Identify the preparation type.
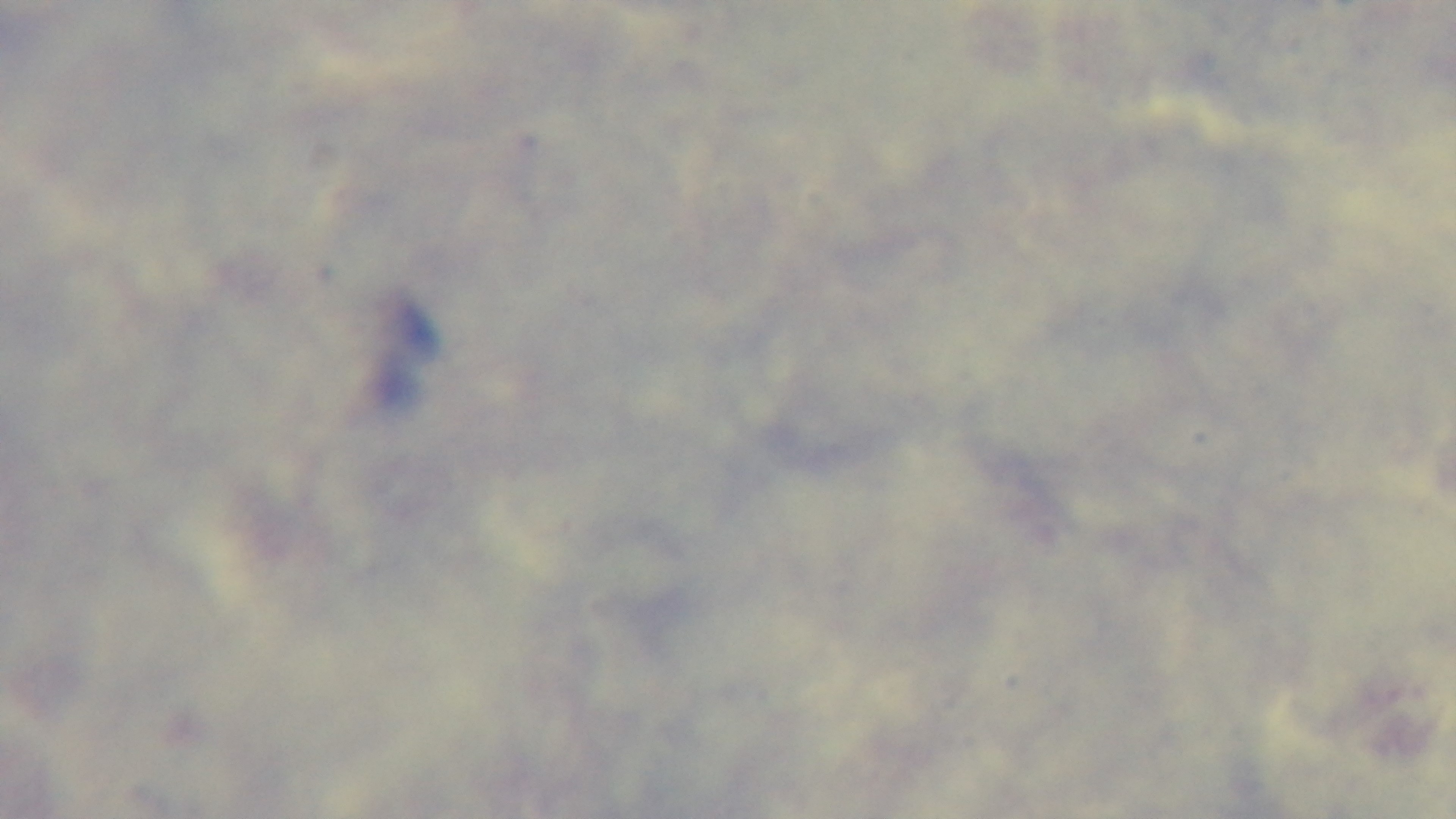
Thick.

Summary:
  - Modality: light microscopy
  - Capture: mounted 4K digital camera
  - Objective: 100x oil immersion
  - Malaria status: negative
  - Stain: Giemsa
  - Field of view: single